Report the malaria status of this cell.
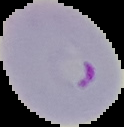

Parasitized.

From a thin blood smear. Cell region segmented out of the field of view; the surrounding area is masked to black. Image is 124×127 pixels.